Locate every Trypanosoma brucei.
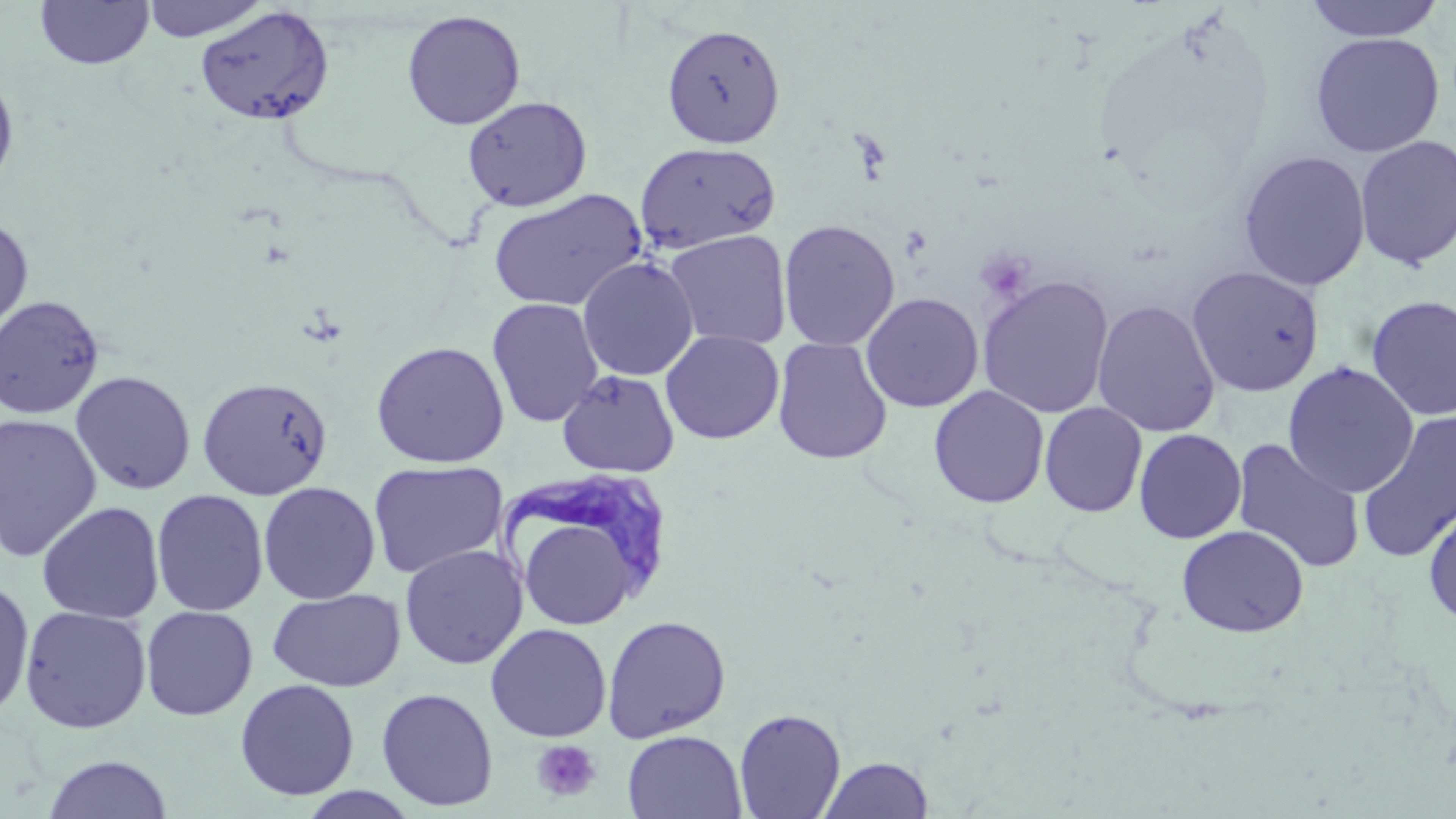
Approximate bounding boxes as (x1, y1, x2, y2) in pixels.
Trypanosoma brucei: (489, 476, 669, 586).

Uninfected red blood cell locations: (35, 0, 154, 69), (141, 0, 269, 42), (1303, 1, 1446, 42), (195, 5, 335, 126), (401, 9, 526, 131), (662, 24, 786, 148), (1310, 32, 1445, 158), (0, 66, 19, 200), (462, 96, 593, 212), (1354, 135, 1456, 271), (635, 141, 781, 254), (1237, 150, 1371, 291), (488, 188, 646, 313), (0, 216, 34, 338), (778, 219, 900, 351), (663, 229, 792, 350), (577, 256, 699, 381), (1185, 265, 1325, 397), (977, 275, 1114, 419), (860, 292, 984, 413), (0, 295, 105, 420), (1366, 295, 1456, 421), (486, 298, 604, 428), (1092, 300, 1220, 438), (660, 330, 784, 445), (772, 337, 893, 465), (370, 340, 509, 468), (1282, 361, 1419, 499), (557, 369, 680, 478), (70, 370, 197, 495), (196, 376, 333, 500), (928, 385, 1049, 508), (1039, 402, 1148, 517), (1357, 411, 1456, 563), (0, 413, 103, 561), (1133, 428, 1247, 544), (1231, 438, 1366, 574), (367, 460, 507, 578), (258, 481, 381, 604), (151, 489, 269, 616), (1422, 498, 1456, 629), (36, 501, 165, 623), (525, 524, 631, 624), (1177, 525, 1309, 637), (399, 544, 527, 669), (0, 578, 35, 721), (267, 588, 406, 692), (19, 605, 152, 733), (140, 605, 258, 721), (601, 614, 731, 743), (485, 623, 611, 743), (234, 678, 360, 801), (376, 687, 498, 811), (733, 707, 846, 819), (623, 730, 747, 818), (42, 754, 173, 818), (819, 755, 934, 818). Platelet locations: (532, 739, 601, 802). Slide-level diagnosis: Trypanosoma brucei. 1000x magnification. Image is 1456×819 pixels. Thin blood smear. Light microscopy. May-Grünwald-Giemsa stain. One field of a larger specimen.